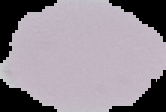
Summary:
  - Result: negative for Plasmodium parasites
  - Preparation: thin blood film
  - Image type: cell region segmented out of the field of view; surrounding area masked to black
  - Image size: 166×112 pixels